Comment on the morphology of the red blood cells.
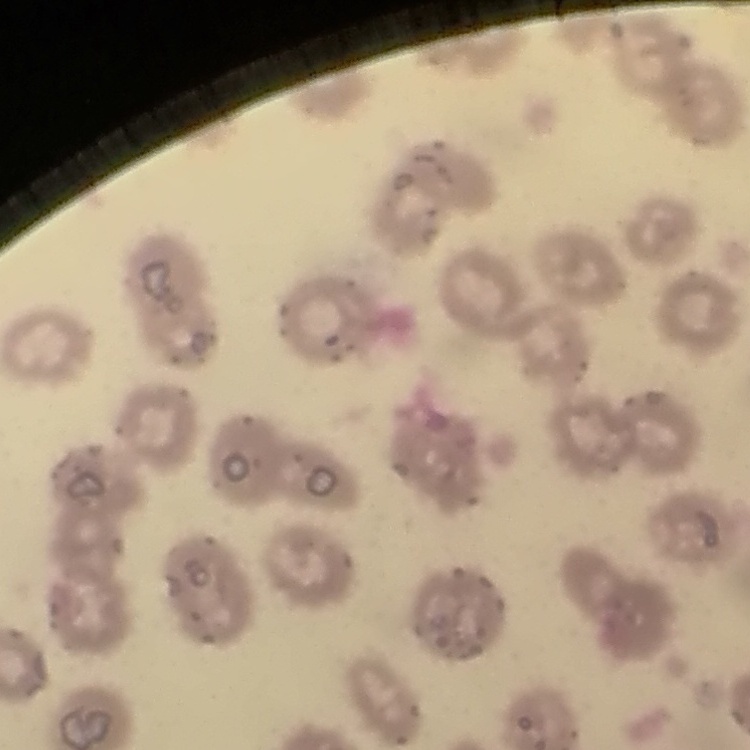
They show no rouleaux formation.

stain = Field's or Giemsa
image type = one tile cut from a larger photomicrograph
preparation = thin peripheral smear